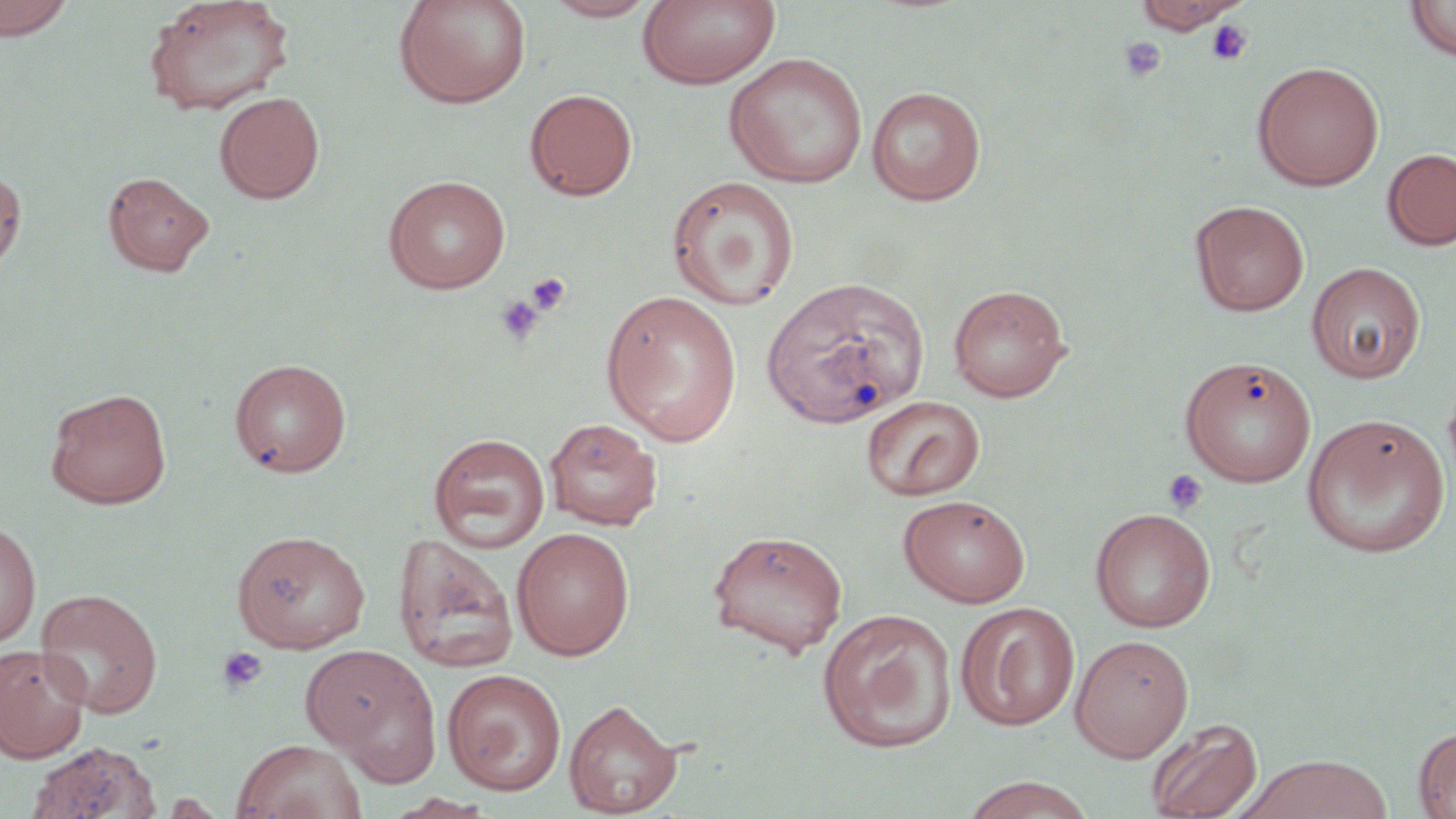
Summary:
  - Coordinate format: approximate bounding boxes as [x1, y1, x2, y2] in pixels
  - Uninfected red blood cell locations: [0, 0, 75, 41], [142, 0, 294, 116], [392, 0, 532, 109], [539, 0, 661, 21], [1404, 0, 1456, 62], [638, 1, 779, 89], [1128, 1, 1247, 33], [724, 53, 868, 188], [1251, 61, 1385, 191], [866, 86, 986, 206], [524, 88, 638, 200], [214, 91, 325, 203], [1382, 148, 1456, 251], [0, 169, 26, 274], [103, 170, 214, 276], [382, 175, 511, 293], [665, 176, 800, 310], [1190, 200, 1310, 317], [1306, 261, 1426, 384], [761, 281, 930, 434], [947, 283, 1071, 402], [601, 290, 742, 446], [228, 357, 352, 477], [1180, 357, 1317, 487], [45, 387, 172, 509], [861, 395, 985, 501], [1301, 413, 1451, 558], [544, 417, 663, 529], [428, 433, 551, 553], [898, 493, 1031, 608], [1089, 507, 1217, 633], [0, 520, 41, 649], [511, 527, 635, 660], [706, 528, 848, 656], [230, 529, 371, 653], [392, 534, 519, 673], [35, 588, 163, 717], [955, 602, 1080, 730], [816, 608, 958, 752], [1070, 634, 1194, 761], [0, 644, 92, 763], [301, 644, 442, 782], [442, 668, 567, 795], [563, 699, 682, 816], [1145, 717, 1263, 819], [1413, 726, 1456, 818], [231, 738, 366, 819], [26, 741, 161, 819], [1238, 754, 1392, 819], [958, 775, 1098, 819], [384, 793, 499, 818]
  - Platelet locations: [1205, 19, 1253, 66], [1119, 38, 1166, 83], [526, 271, 572, 315], [495, 294, 544, 346], [1162, 468, 1208, 516], [216, 646, 267, 694]
  - Slide-level diagnosis: no evidence of blood parasites
  - Image size: 1456×819 pixels
  - Modality: light microscopy
  - Stain: May-Grünwald-Giemsa
  - Magnification: 1000x
  - Field of view: single
  - Preparation: thin blood smear